Assess this cell for malaria.
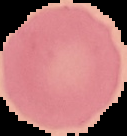

Uninfected.

image_type: segmented cell region on a black background
image_size: 127×136 pixels
preparation: thin blood film